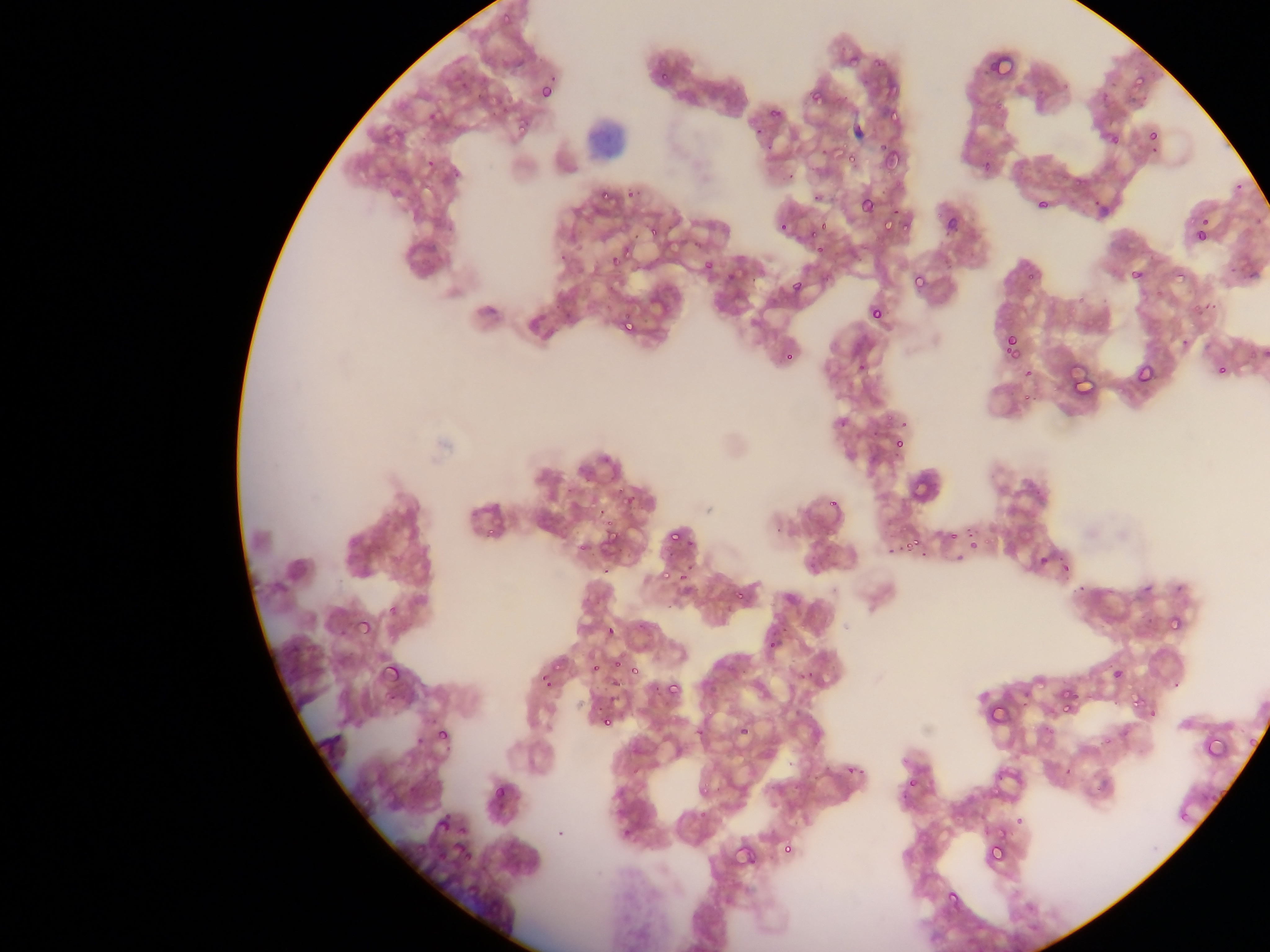
artifact (stain precipitate or debris) locations = approximate bounding boxes as left top right bottom in pixels: 585 108 640 156
country = Ghana
malaria parasite locations = approximate bounding boxes as left top right bottom in pixels: 495 9 508 23; 850 44 867 62; 986 51 1019 83; 876 52 898 72; 1131 72 1149 90; 811 74 835 104; 538 81 559 104; 483 89 509 112; 889 100 907 123; 512 121 534 139; 1150 126 1174 153; 842 138 863 165; 879 142 906 170; 423 155 440 175; 597 190 613 201; 858 194 878 217; 1034 194 1054 214; 877 213 900 231; 942 215 960 237; 646 222 665 243; 1193 226 1211 245; 556 252 570 265; 610 256 624 270; 699 257 718 278; 722 266 740 286; 1176 269 1191 282; 909 270 930 294; 1128 270 1141 280; 788 276 808 299; 868 302 889 324; 619 314 643 335; 1003 336 1021 358; 782 351 796 366; 1133 361 1158 389; 1071 370 1102 391; 888 430 914 459; 891 436 908 455; 911 479 927 499; 827 487 843 508; 621 492 639 511; 944 507 967 542; 484 512 505 539; 601 524 624 551; 665 526 687 548; 904 532 924 550; 1035 552 1053 571; 1059 560 1073 577; 661 566 673 579; 731 590 741 600; 354 608 378 632; 1166 615 1183 632; 604 624 618 639; 379 656 407 686; 626 657 646 680; 554 658 571 675; 590 662 603 675; 1108 663 1124 684; 661 679 683 702; 1058 687 1088 722; 1125 691 1142 707; 989 703 1014 723; 598 712 618 731; 733 713 754 736; 436 721 454 742; 1203 733 1233 761; 1246 734 1263 755; 897 761 926 795; 490 781 512 806; 429 808 453 837; 1180 812 1190 824; 988 823 1010 840; 410 833 439 855; 451 835 470 858; 985 838 1009 866; 733 839 754 869; 780 842 797 852; 948 891 964 908
preparation = thin blood film
image size = 1270×952 pixels
capture = mobile-phone photograph through a microscope
field of view = single